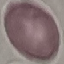

result = negative for malaria parasites
image type = cell patch, automatically extracted from a larger field of view and resized to 64 × 64 pixels
capture = smartphone through the microscope eyepiece
preparation = thin blood film
stain = Giemsa